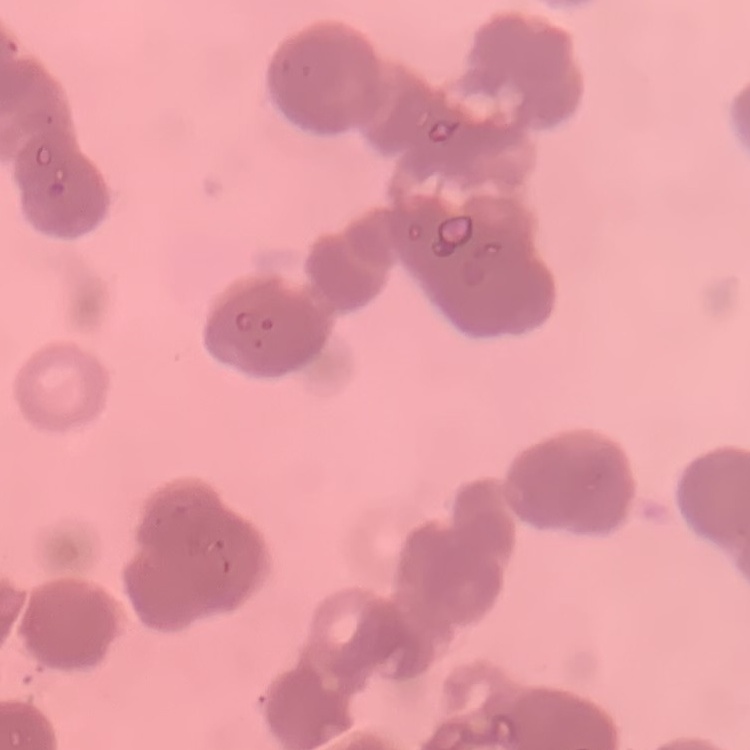

Summary:
  - Red blood cell morphology: rouleaux formation
  - Preparation: thin peripheral smear
  - Stain: Field's or Giemsa
  - Image type: one tile cut from a larger photomicrograph